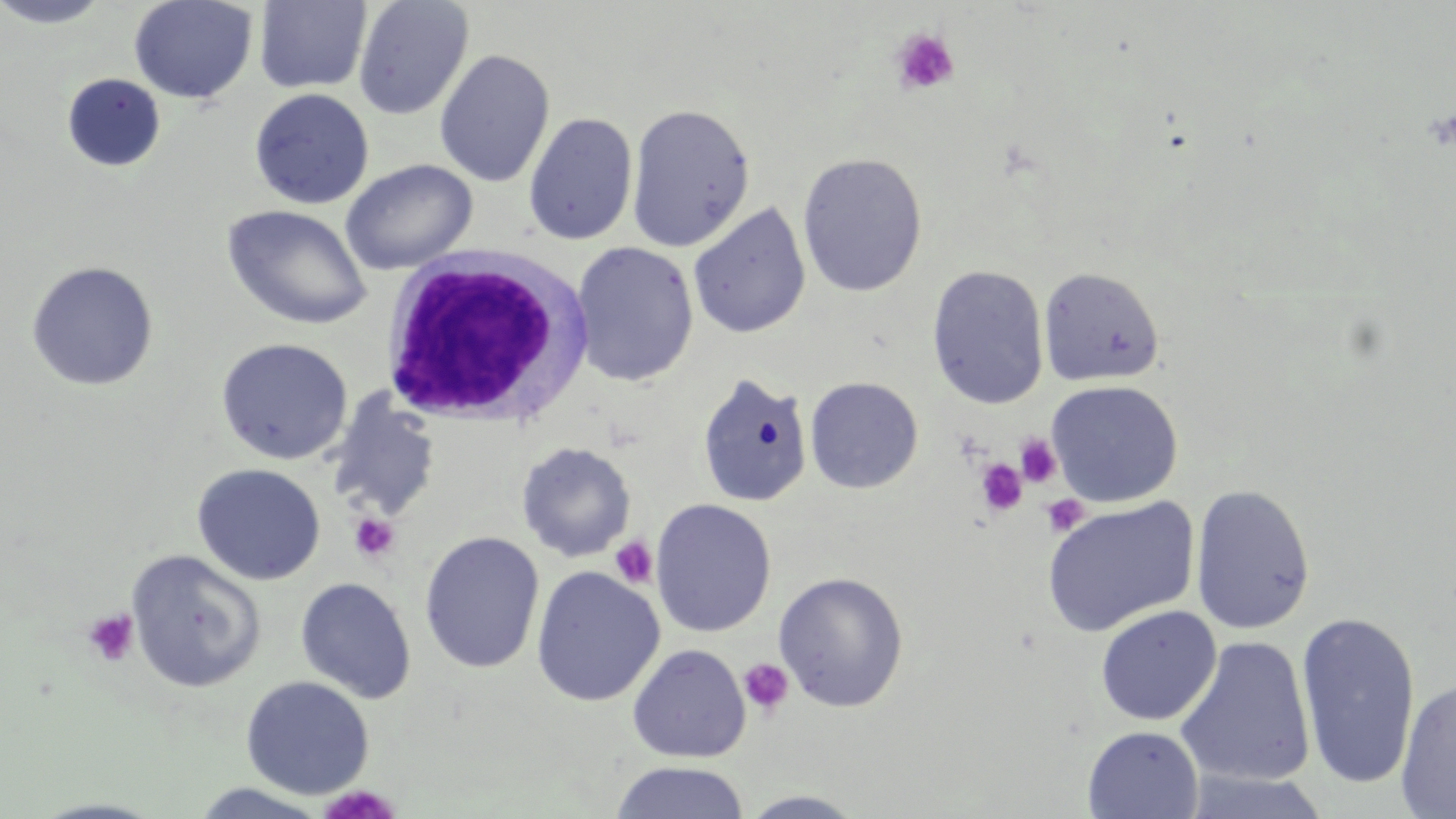

Summary:
  - Coordinate format: approximate bounding boxes as named x1/y1/x2/y2 corners in pixels
  - White blood cell locations: (x1=377, y1=249, x2=597, y2=431)
  - Platelet locations: (x1=891, y1=28, x2=961, y2=97), (x1=1014, y1=434, x2=1062, y2=488), (x1=975, y1=457, x2=1028, y2=517), (x1=1041, y1=493, x2=1090, y2=537), (x1=348, y1=512, x2=400, y2=563), (x1=609, y1=536, x2=658, y2=589), (x1=82, y1=609, x2=139, y2=666), (x1=738, y1=657, x2=794, y2=716), (x1=317, y1=785, x2=403, y2=819)
  - Uninfected red blood cell locations: (x1=0, y1=0, x2=114, y2=28), (x1=129, y1=0, x2=258, y2=104), (x1=254, y1=1, x2=372, y2=94), (x1=353, y1=1, x2=473, y2=120), (x1=434, y1=49, x2=555, y2=187), (x1=62, y1=73, x2=165, y2=172), (x1=249, y1=88, x2=374, y2=209), (x1=626, y1=103, x2=756, y2=252), (x1=523, y1=112, x2=638, y2=245), (x1=797, y1=152, x2=928, y2=297), (x1=340, y1=159, x2=478, y2=275), (x1=688, y1=202, x2=811, y2=340), (x1=222, y1=205, x2=372, y2=330), (x1=570, y1=241, x2=699, y2=386), (x1=25, y1=260, x2=159, y2=391), (x1=926, y1=265, x2=1050, y2=410), (x1=1038, y1=266, x2=1165, y2=388), (x1=215, y1=336, x2=353, y2=465), (x1=695, y1=373, x2=814, y2=507), (x1=805, y1=377, x2=923, y2=494), (x1=1046, y1=380, x2=1183, y2=506), (x1=327, y1=390, x2=442, y2=523), (x1=516, y1=442, x2=636, y2=562), (x1=191, y1=463, x2=326, y2=585), (x1=1190, y1=483, x2=1315, y2=636), (x1=1041, y1=497, x2=1200, y2=637), (x1=649, y1=498, x2=777, y2=637), (x1=419, y1=532, x2=544, y2=674), (x1=126, y1=550, x2=267, y2=693), (x1=530, y1=565, x2=665, y2=707), (x1=772, y1=571, x2=909, y2=712), (x1=295, y1=577, x2=417, y2=704), (x1=1095, y1=605, x2=1222, y2=726), (x1=1295, y1=612, x2=1421, y2=790), (x1=1175, y1=636, x2=1316, y2=788), (x1=627, y1=644, x2=751, y2=763), (x1=240, y1=675, x2=375, y2=799), (x1=1395, y1=677, x2=1456, y2=819), (x1=1082, y1=725, x2=1204, y2=818), (x1=610, y1=761, x2=750, y2=819), (x1=189, y1=782, x2=332, y2=817), (x1=736, y1=790, x2=869, y2=818), (x1=26, y1=796, x2=172, y2=818)
  - Slide-level diagnosis: negative for blood parasites
  - Modality: light microscopy
  - Stain: May-Grünwald-Giemsa
  - Preparation: thin blood film
  - Field of view: single
  - Image size: 1456×819 pixels
  - Magnification: 1000x